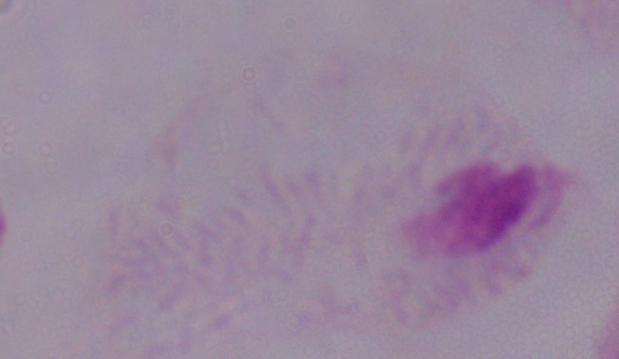
1000x magnification. Micrograph. A trichomonad is seen.